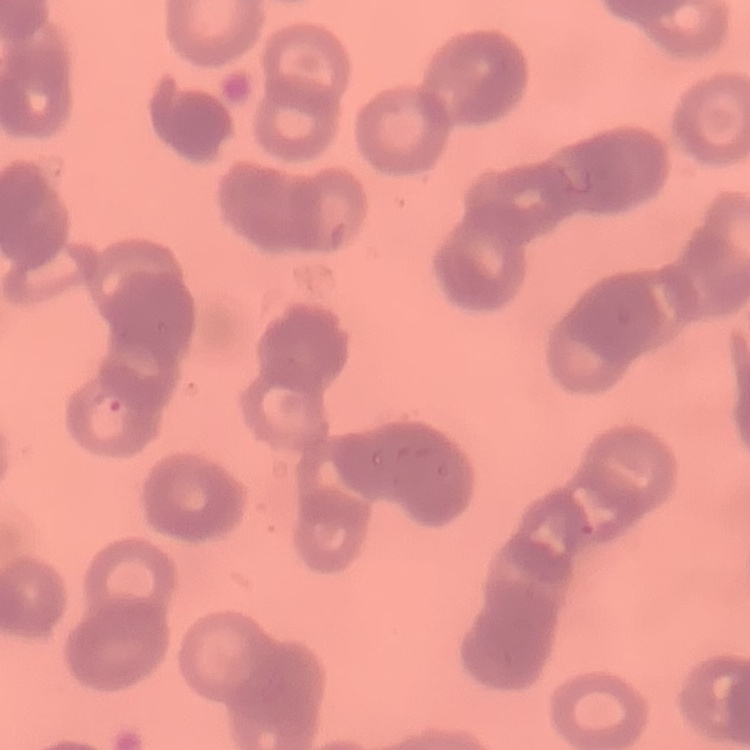

red blood cell morphology = rouleaux formation
preparation = thin peripheral smear
image type = square crop of a larger photomicrograph
stain = Field's or Giemsa